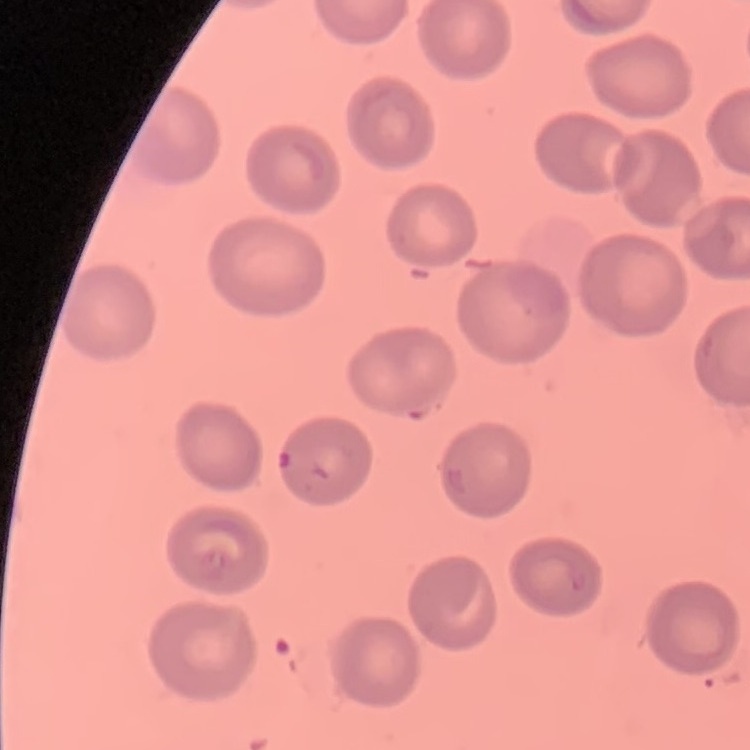

red_blood_cell_morphology: no rouleaux formation
preparation: thin peripheral smear
stain: Field's or Giemsa
image_type: square crop of a larger photomicrograph